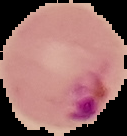

The area outside the segmented cell region is set to black. Malaria status: parasitized. From a thin blood film. Image is 127×136 pixels.